Outline every malaria parasite, every leukocyte, and every artifact (stain precipitate or debris).
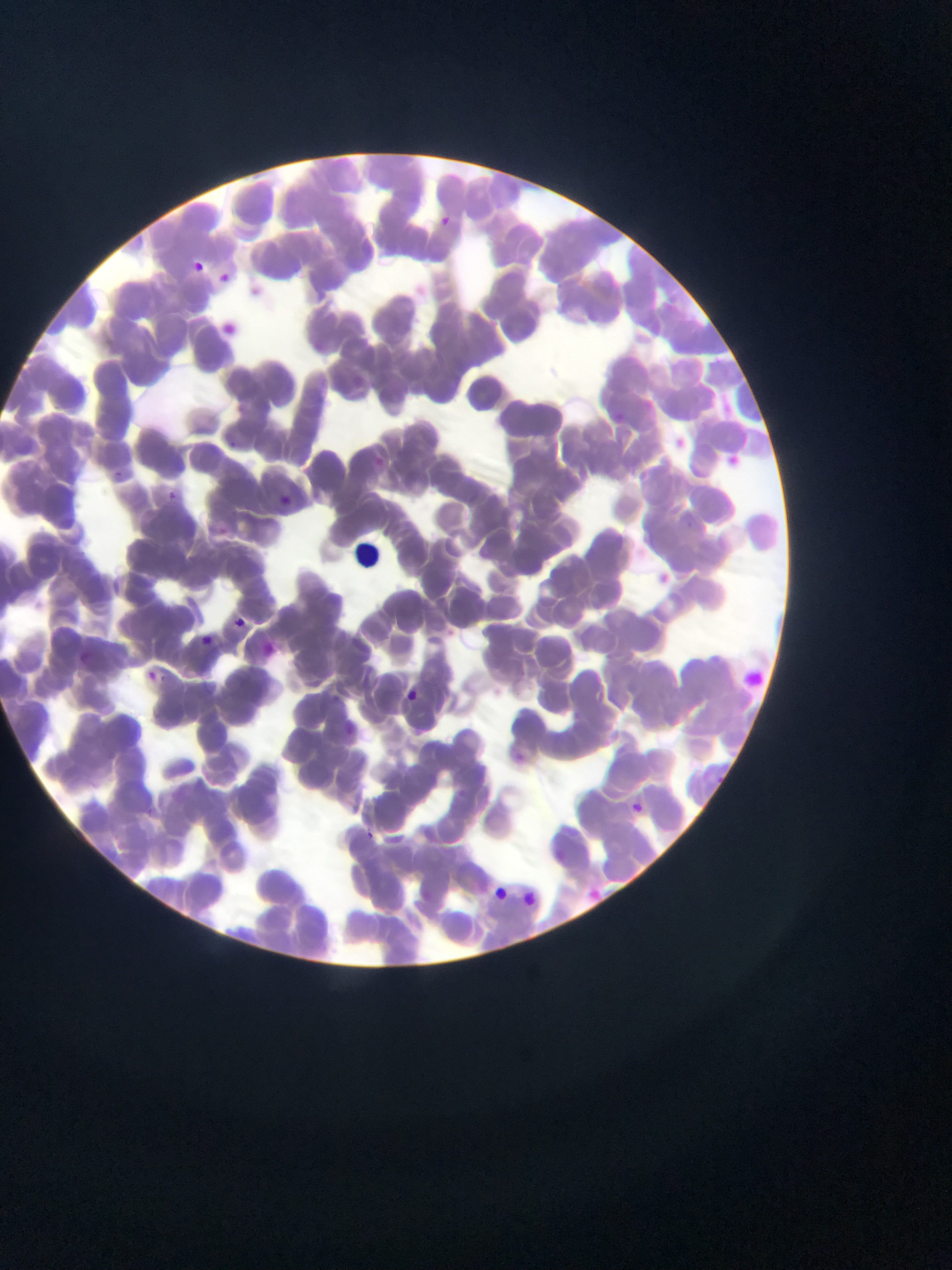

Approximate bounding boxes as [left, top, right, bottom] in pixels.
Malaria parasites: [433, 210, 457, 233], [185, 257, 208, 278], [214, 265, 237, 288], [246, 280, 267, 300], [663, 428, 698, 464], [724, 448, 745, 478], [165, 489, 180, 504], [275, 492, 295, 510], [653, 567, 675, 588], [228, 611, 253, 634], [196, 631, 216, 650], [253, 635, 288, 658], [739, 656, 772, 697], [401, 686, 423, 706], [625, 799, 648, 820], [496, 871, 521, 901], [578, 878, 604, 901], [519, 885, 559, 905].
Leukocytes: [352, 526, 413, 582], [336, 719, 372, 739].

{
  "country": "Ghana",
  "preparation": "thin blood smear",
  "image_size": "952×1270 pixels",
  "field_of_view": "single",
  "capture": "mobile-phone photograph through a microscope"
}